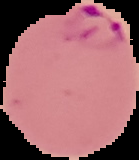

image type = segmented cell region on a black background
malaria status = parasitized
preparation = thin blood smear
image size = 139×160 pixels